Locate every blood parasite and identify its species.
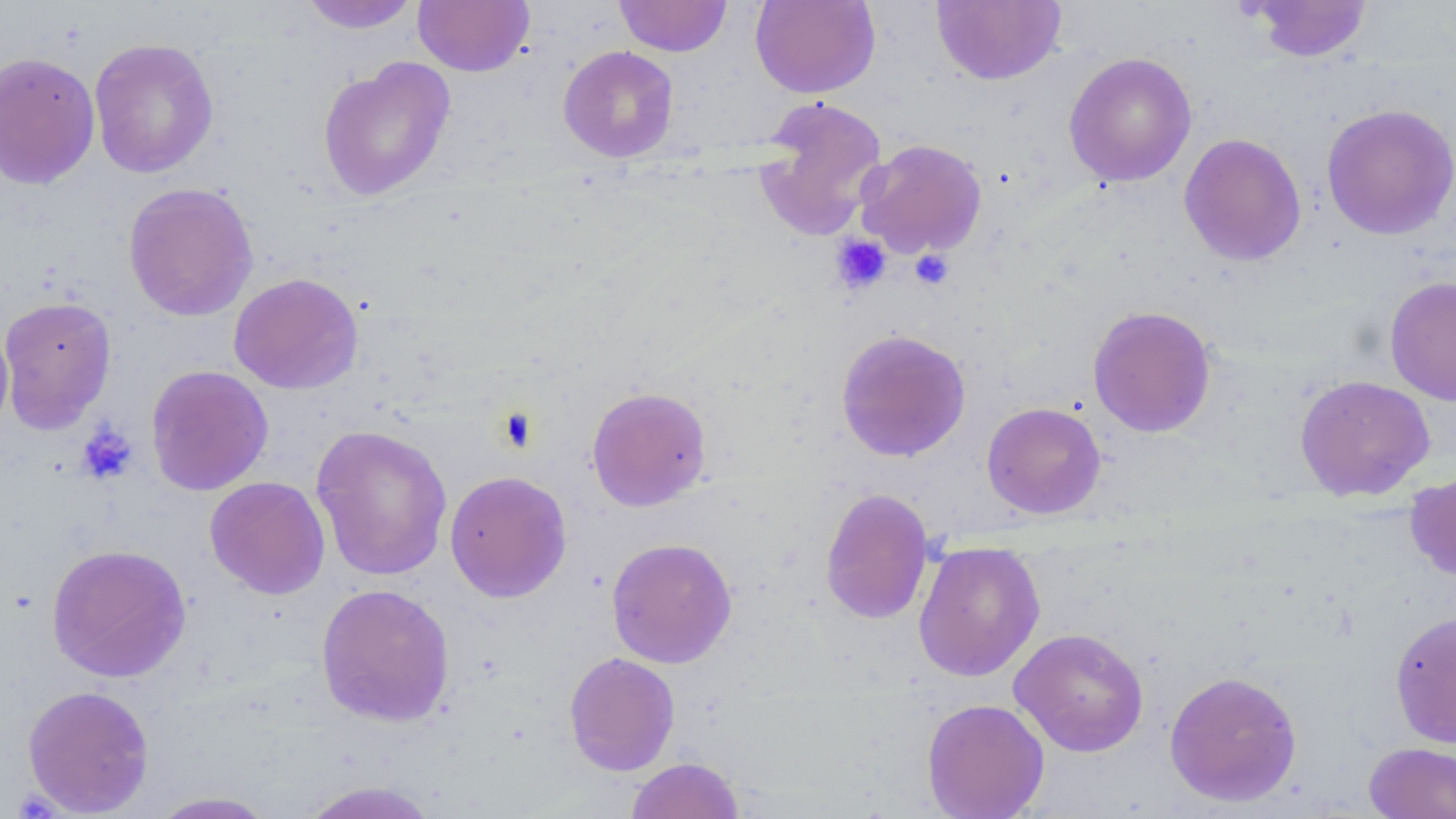
No blood parasites seen.

Approximate bounding boxes as [x1, y1, x2, y2] in pixels. Uninfected red blood cell locations: [297, 0, 423, 33], [413, 0, 534, 76], [614, 0, 732, 57], [750, 0, 880, 98], [931, 0, 1066, 85], [1247, 1, 1373, 62], [88, 38, 219, 178], [558, 45, 679, 163], [0, 51, 101, 190], [1064, 51, 1197, 187], [317, 57, 456, 202], [753, 96, 889, 240], [1321, 103, 1456, 240], [1179, 133, 1306, 266], [855, 138, 988, 259], [122, 182, 258, 321], [228, 272, 364, 395], [1385, 276, 1456, 406], [0, 296, 117, 433], [1087, 305, 1217, 438], [0, 316, 14, 435], [835, 329, 972, 462], [146, 364, 273, 496], [1294, 374, 1435, 502], [586, 386, 712, 511], [982, 401, 1106, 519], [311, 424, 453, 581], [445, 470, 572, 602], [1405, 470, 1456, 583], [204, 476, 330, 599], [820, 487, 934, 625], [606, 537, 738, 669], [913, 541, 1046, 682], [46, 543, 191, 683], [315, 582, 455, 727], [1389, 611, 1456, 748], [1009, 627, 1149, 756], [564, 651, 680, 776], [1378, 652, 1454, 816], [1164, 670, 1303, 807], [22, 684, 155, 816], [921, 698, 1050, 819], [1363, 742, 1455, 819], [625, 757, 745, 819], [297, 780, 443, 818], [147, 791, 280, 818]. Platelet locations: [831, 234, 892, 295], [909, 249, 954, 290], [493, 406, 541, 454], [76, 422, 138, 485]. Slide-level diagnosis: no evidence of blood parasites. One field of a larger specimen. Thin blood film. May-Grünwald-Giemsa-stained preparation. Captured at 1000x magnification. Optical microscopy. Image is 1456×819 pixels.